Locate every blood parasite and identify its species.
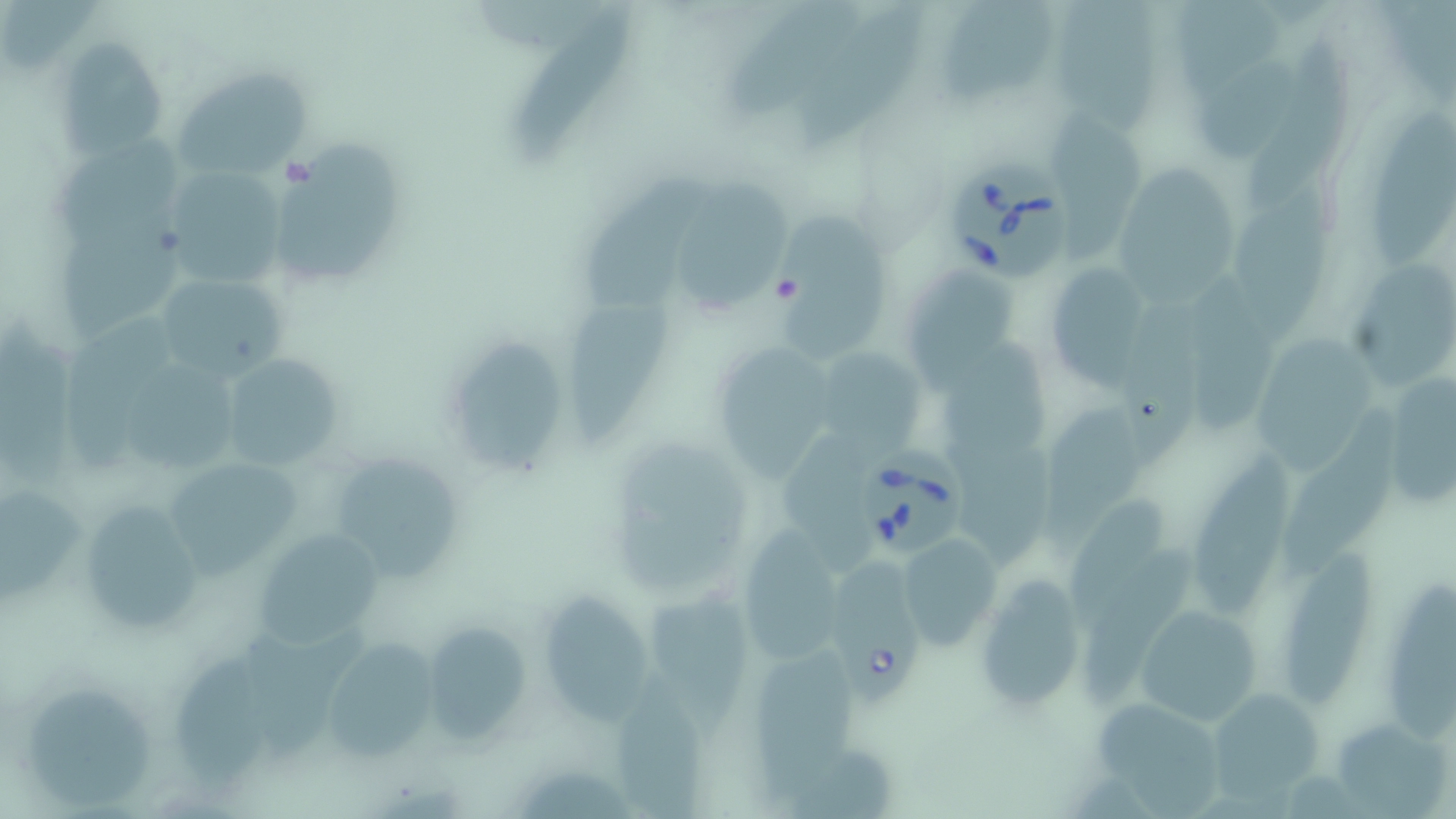
Approximate bounding boxes as (x1, y1, x2, y2) in pixels.
Babesia divergens-infected red blood cells: (948, 162, 1077, 283), (860, 446, 966, 559), (834, 558, 927, 710).
No Plasmodium falciparum, Plasmodium ovale, Plasmodium malariae, Plasmodium vivax, or Trypanosoma brucei observed.

Uninfected red blood cell locations: (0, 0, 103, 72), (722, 0, 862, 129), (1052, 0, 1166, 136), (792, 2, 929, 154), (942, 3, 1055, 109), (1182, 4, 1287, 95), (514, 16, 642, 154), (55, 37, 172, 160), (1249, 40, 1354, 202), (1197, 61, 1300, 162), (171, 65, 314, 185), (1367, 99, 1456, 268), (1045, 108, 1147, 264), (52, 135, 188, 237), (274, 141, 406, 286), (1121, 161, 1246, 316), (161, 164, 294, 288), (573, 173, 708, 312), (674, 174, 794, 319), (1240, 193, 1334, 327), (778, 199, 889, 361), (62, 210, 193, 336), (1044, 256, 1158, 388), (1344, 256, 1455, 386), (896, 266, 1023, 390), (1178, 266, 1293, 438), (147, 268, 295, 383), (1120, 290, 1211, 464), (559, 297, 676, 440), (67, 310, 181, 465), (0, 322, 86, 489), (1254, 327, 1382, 472), (710, 338, 832, 475), (452, 340, 571, 470), (811, 345, 925, 455), (945, 346, 1055, 477), (220, 351, 347, 478), (125, 358, 239, 476), (1373, 369, 1456, 515), (1042, 399, 1146, 545), (1281, 409, 1411, 580), (779, 429, 877, 562), (616, 436, 757, 590), (961, 442, 1054, 564), (1190, 443, 1298, 614), (334, 454, 467, 587), (159, 455, 306, 577), (0, 484, 91, 613), (73, 496, 205, 636), (1072, 496, 1172, 611), (250, 527, 388, 649), (735, 533, 846, 663), (899, 533, 1004, 654), (1087, 546, 1199, 719), (1278, 552, 1378, 711), (974, 572, 1088, 713), (1385, 574, 1456, 748), (542, 581, 650, 729), (648, 593, 759, 743), (1131, 602, 1265, 726), (424, 620, 535, 742), (316, 636, 445, 762), (171, 654, 269, 789), (757, 661, 862, 795), (614, 680, 717, 819), (26, 682, 156, 810), (1205, 687, 1323, 804), (1085, 696, 1227, 814), (1333, 714, 1449, 819). Platelet locations: (771, 272, 803, 304). Slide-level diagnosis: Babesia divergens. May-Grünwald-Giemsa stain. Thin blood film. Image is 1456×819 pixels. Light microscopy. 1000x magnification. Single field of view.